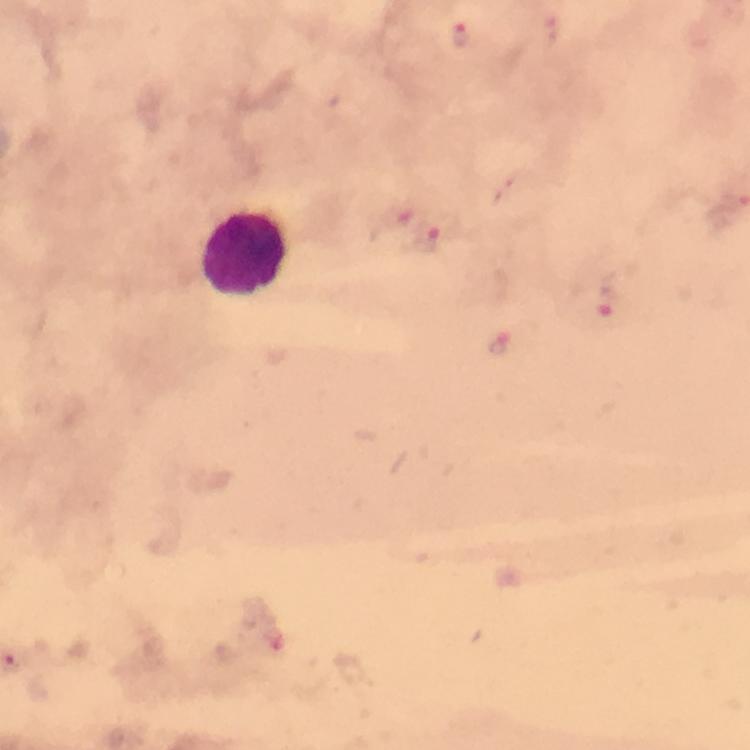

Approximate centers as {x, y} in pixels. Leukocyte locations: {243, 253}. Plasmodium parasite locations: {462, 35}, {428, 238}, {608, 302}, {500, 345}. Thick blood smear. Giemsa stain. Smartphone photograph taken through a microscope. Cropped region of a single field of view. 100x magnification. Immersion oil was used. Image is 750×750 pixels. From a diagnostic examination for malaria.